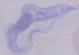

Summary:
  - Identification: trypanosome
  - Magnification: 1000x
  - Modality: micrograph